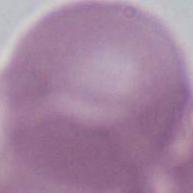
Summary:
  - Modality: photomicrograph
  - Magnification: 1000x
  - Identification: erythrocyte